Identify the parasite.
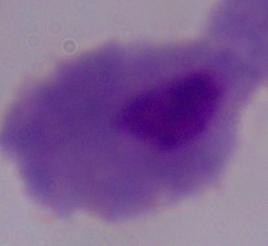
This is a trichomonad.

Captured at 1000x magnification. Photomicrograph.